Assess this cell for malaria.
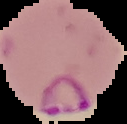

Parasitized.

Summary:
  - Image size: 127×124 pixels
  - Image type: segmented cell region with the area outside set to black
  - Preparation: thin blood smear